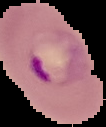
{
  "preparation": "thin blood smear",
  "image_size": "106×127 pixels",
  "result": "malaria parasites identified",
  "image_type": "segmented cell region with the area outside set to black"
}